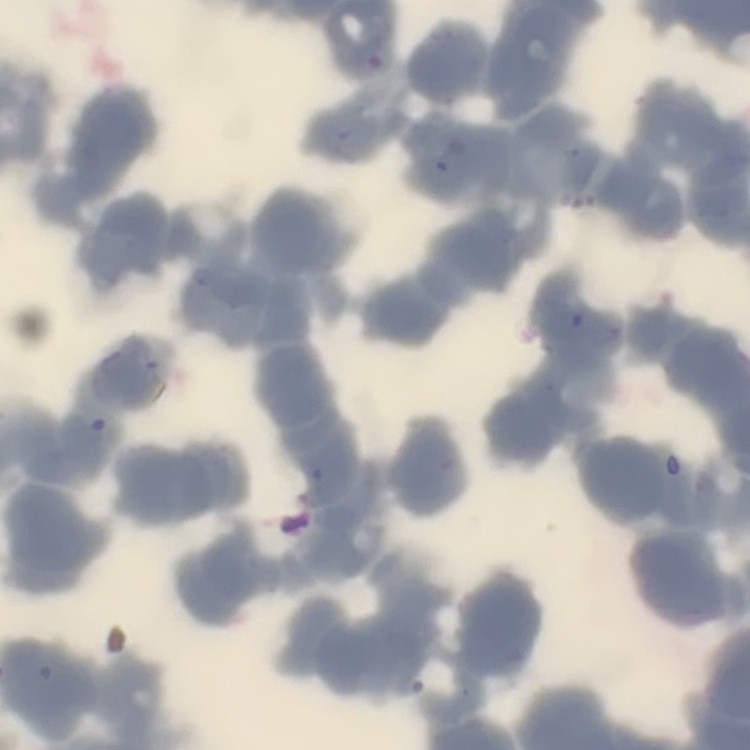

The red blood cells show rouleaux formation. Field's or Giemsa stain. One tile cut from a larger photomicrograph. Thin peripheral smear.